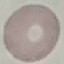
{
  "malaria_status": "uninfected",
  "capture": "smartphone camera at the microscope eyepiece",
  "stain": "Giemsa",
  "image_type": "automatically extracted cell patch, resized to 64 × 64 pixels",
  "preparation": "thin blood film"
}